Classify this cell by malaria status.
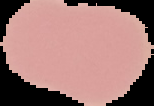

It is uninfected.

Summary:
  - Image size: 154×106 pixels
  - Preparation: thin blood film
  - Image type: segmented cell region on a black background